State which cell type is depicted.
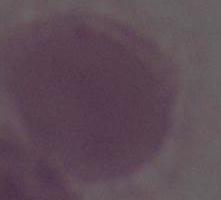
An erythrocyte.

Photomicrograph. 1000x magnification.